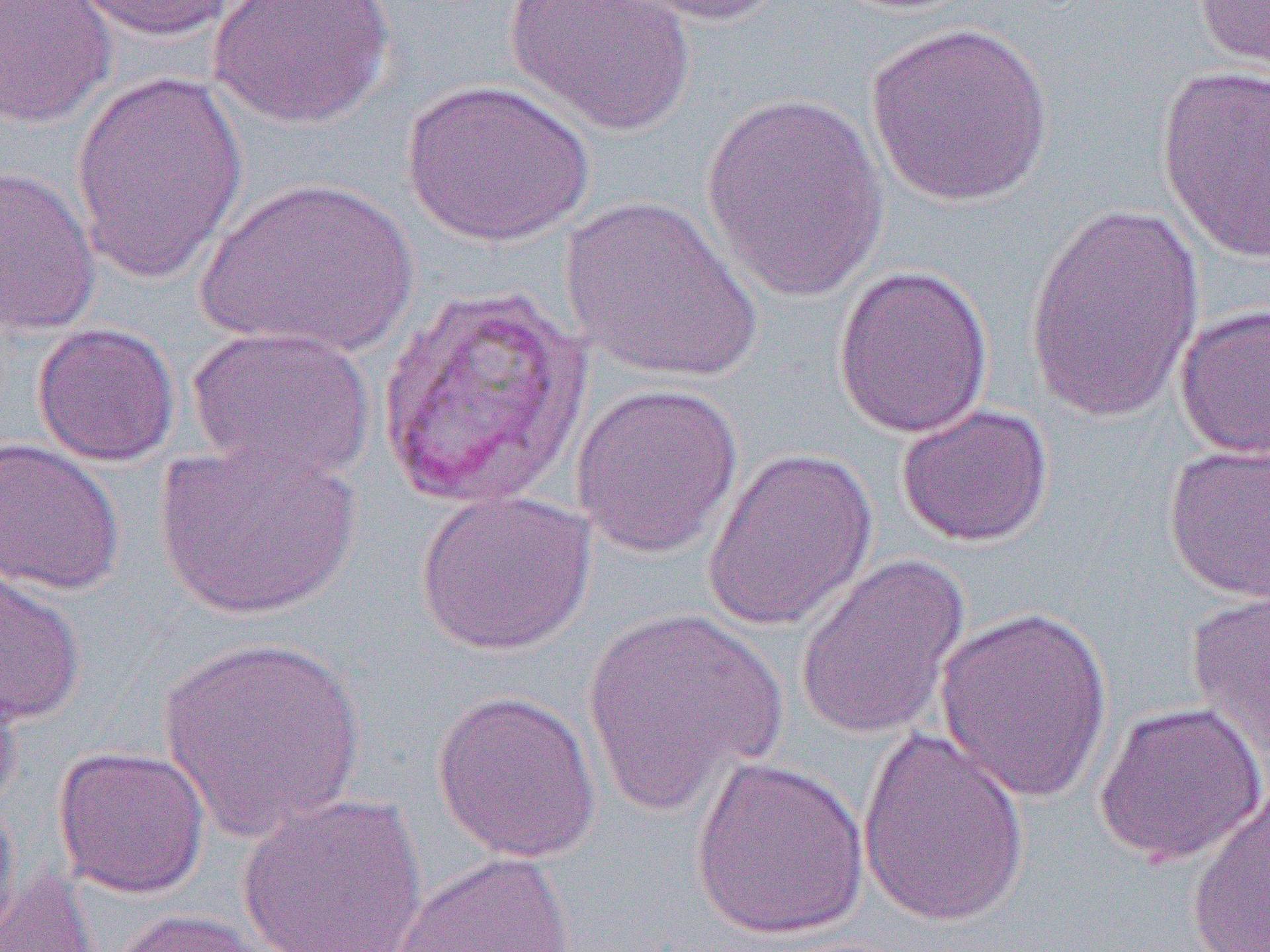

slide-level diagnosis = Plasmodium vivax
image size = 1270×952 pixels
magnification = 1000x
preparation = thin blood film
field of view = single
uninfected red blood cell locations = approximate bounding boxes as named x1/y1/x2/y2 corners in pixels: (x1=0, y1=0, x2=117, y2=128), (x1=68, y1=0, x2=245, y2=41), (x1=208, y1=0, x2=395, y2=130), (x1=504, y1=0, x2=696, y2=137), (x1=617, y1=0, x2=794, y2=27), (x1=1194, y1=0, x2=1269, y2=75), (x1=865, y1=21, x2=1055, y2=208), (x1=1156, y1=66, x2=1269, y2=264), (x1=70, y1=69, x2=249, y2=285), (x1=401, y1=78, x2=595, y2=248), (x1=699, y1=92, x2=892, y2=303), (x1=0, y1=165, x2=102, y2=337), (x1=196, y1=177, x2=419, y2=358), (x1=560, y1=195, x2=763, y2=385), (x1=1022, y1=202, x2=1206, y2=422), (x1=832, y1=265, x2=994, y2=439), (x1=1173, y1=302, x2=1270, y2=461), (x1=32, y1=322, x2=180, y2=467), (x1=185, y1=325, x2=375, y2=485), (x1=570, y1=382, x2=743, y2=559), (x1=895, y1=403, x2=1055, y2=548), (x1=0, y1=436, x2=125, y2=596), (x1=153, y1=438, x2=363, y2=622), (x1=1163, y1=441, x2=1270, y2=604), (x1=701, y1=446, x2=879, y2=632), (x1=414, y1=489, x2=596, y2=656), (x1=794, y1=552, x2=970, y2=741), (x1=0, y1=562, x2=87, y2=727), (x1=1186, y1=590, x2=1270, y2=761), (x1=581, y1=606, x2=787, y2=816), (x1=933, y1=606, x2=1114, y2=804), (x1=155, y1=636, x2=368, y2=842), (x1=0, y1=667, x2=23, y2=819), (x1=430, y1=689, x2=601, y2=863), (x1=1093, y1=700, x2=1266, y2=868), (x1=855, y1=727, x2=1031, y2=930), (x1=52, y1=745, x2=210, y2=898), (x1=689, y1=755, x2=870, y2=941), (x1=1186, y1=781, x2=1269, y2=952), (x1=236, y1=791, x2=429, y2=952), (x1=0, y1=795, x2=22, y2=940), (x1=390, y1=850, x2=577, y2=952), (x1=0, y1=865, x2=101, y2=952), (x1=104, y1=908, x2=281, y2=952)
modality = light microscopy